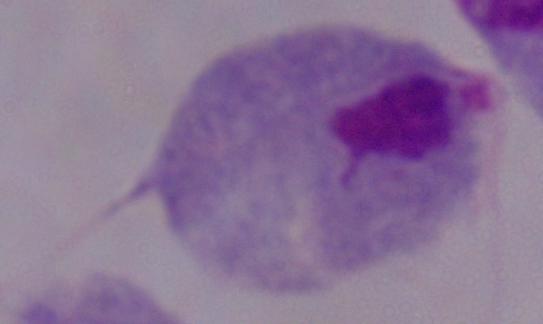

modality = micrograph
magnification = 1000x
identification = trichomonad